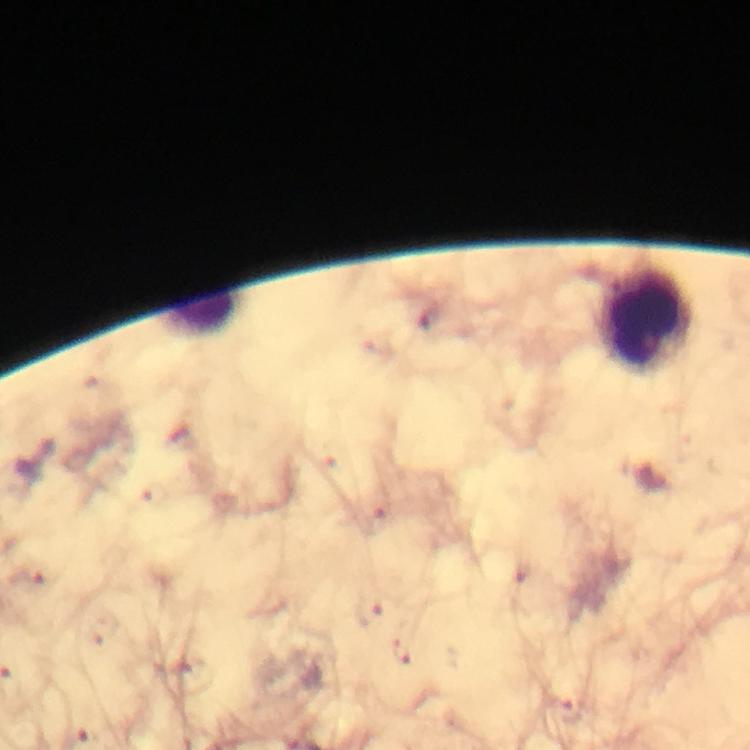 Approximate centers as {x, y} in pixels. Malaria parasite locations: {403, 651}. Leukocyte locations: {207, 313}, {645, 322}. Thick blood smear. Giemsa-stained preparation. Image is 750×750 pixels. 100x magnification. Smartphone photograph taken through a microscope. From a malaria diagnostic workup. A crop from one field of view. Immersion oil was used.